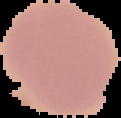
{
  "preparation": "thin blood film",
  "malaria_status": "uninfected",
  "image_size": "121×118 pixels",
  "image_type": "cell region segmented out of the field of view; surrounding area masked to black"
}